Give the preparation type.
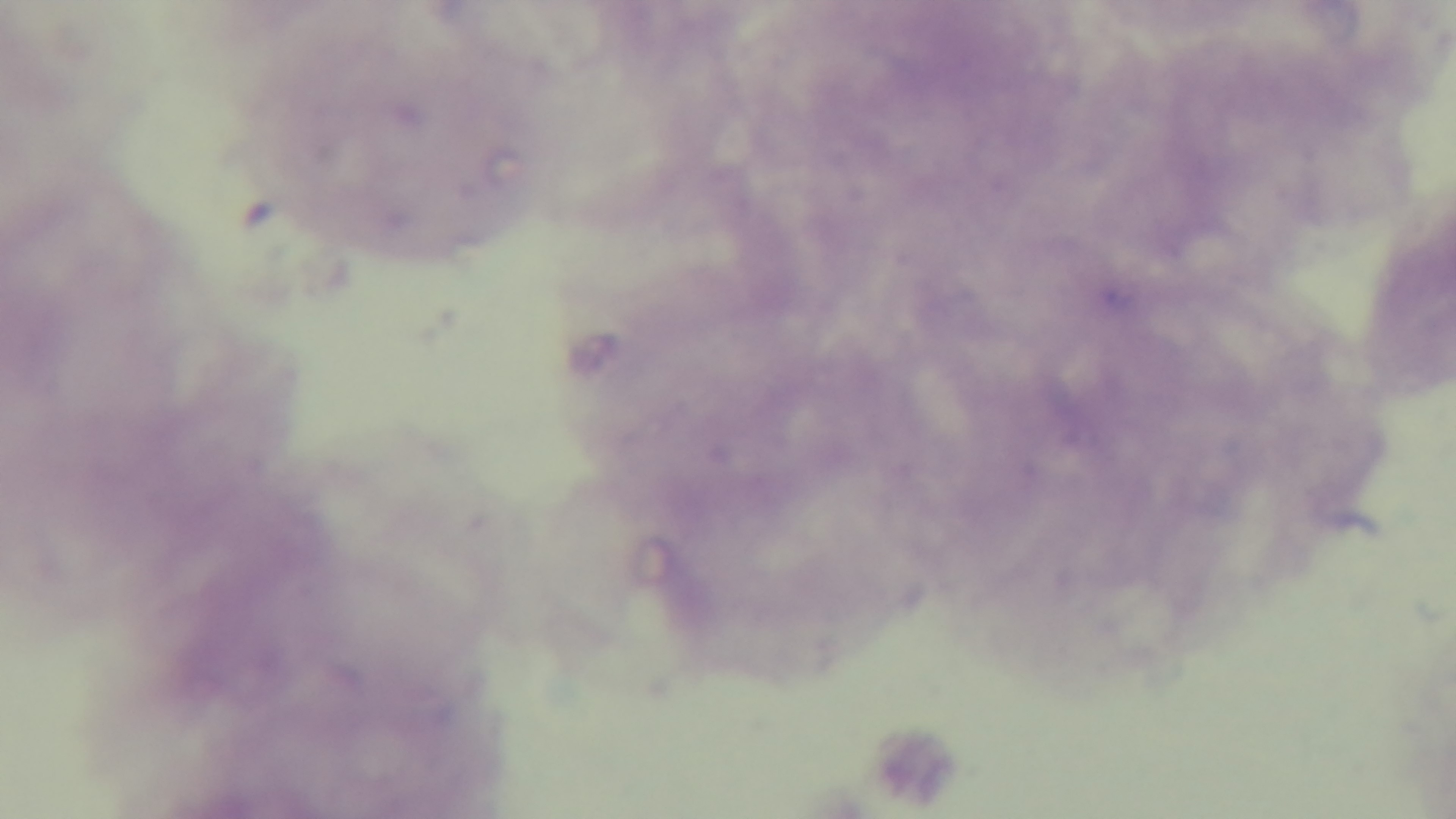
A thick smear.

Giemsa-stained. Malaria status: uninfected. 100x oil-immersion objective. Light microscopy. One field from the slide. Mounted 4K digital camera.